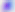
Summary:
  - Magnification: 400x
  - Identification: Toxoplasma gondii
  - Modality: micrograph